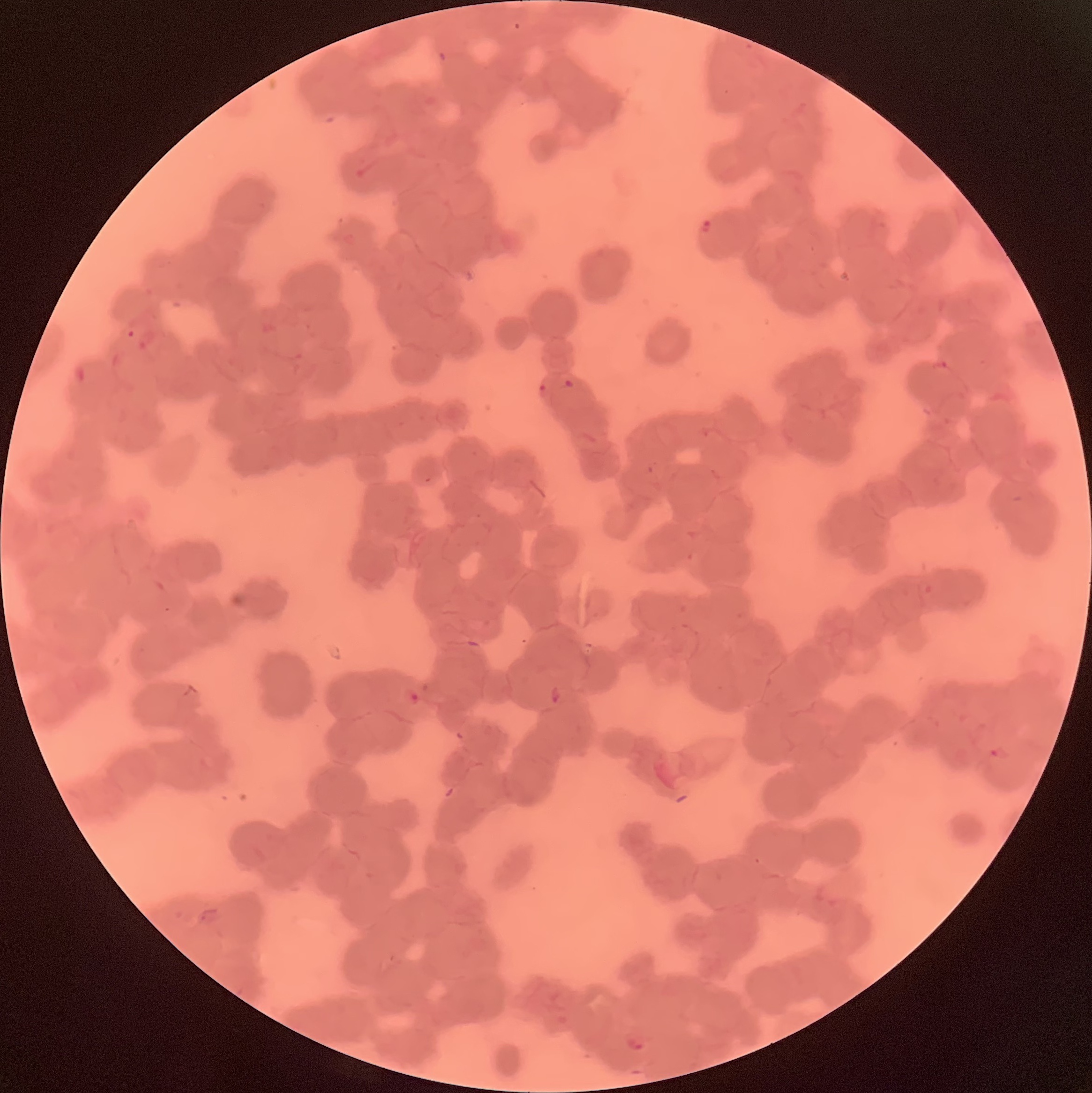
Approximate bounding boxes as (x1, y1, x2, y2) in pixels. Plasmodium parasite locations: (701, 220, 711, 233), (563, 379, 574, 388), (539, 382, 553, 404), (550, 685, 561, 704), (403, 689, 420, 705), (988, 745, 1010, 762), (624, 1036, 645, 1053). Optical microscopy. The red blood cells show rouleaux formation. Image is 1092×1093 pixels. Thin blood smear.